Assess the morphology of the red blood cells.
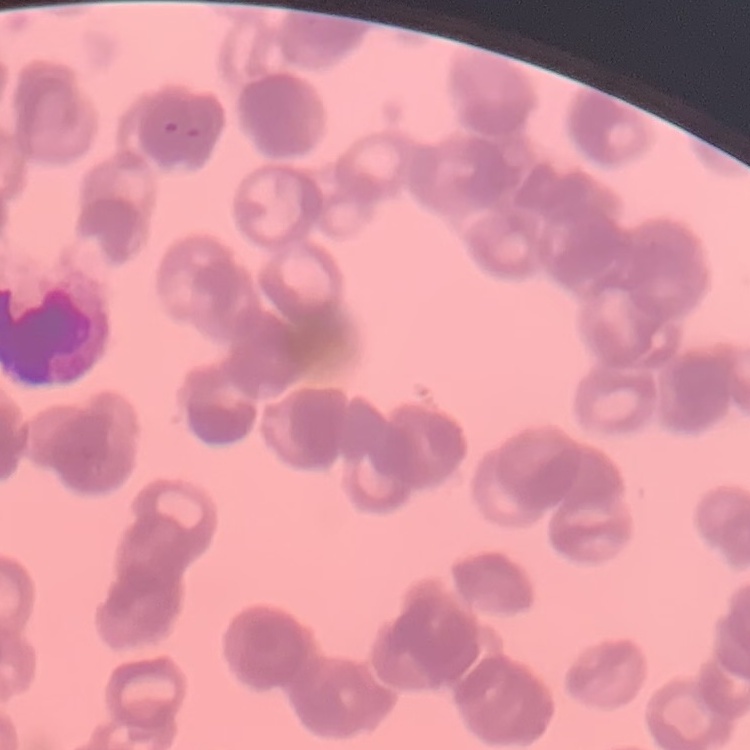
Rouleaux formation.

One tile cut from a larger photomicrograph. Thin blood smear. Stained with either Field's or Giemsa.